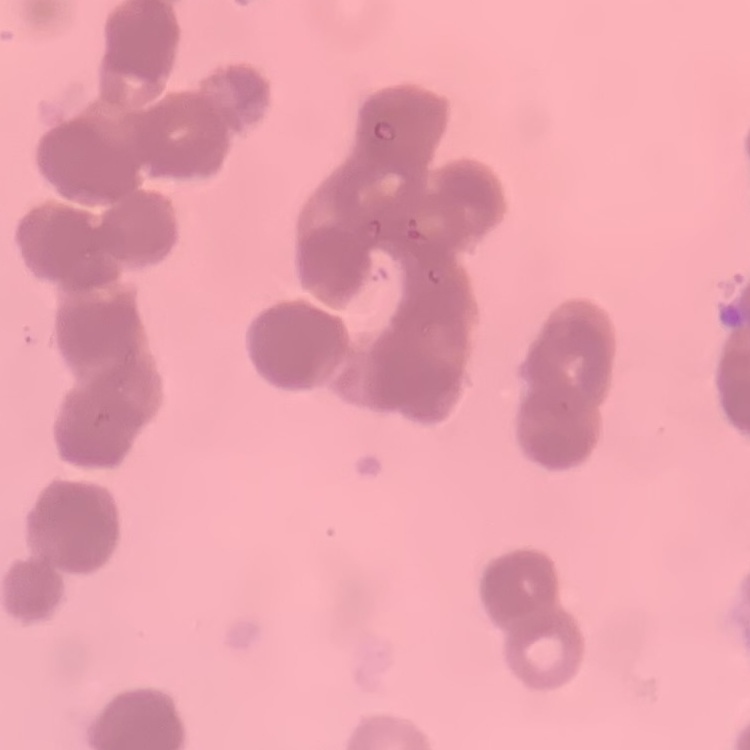

{
  "erythrocyte_morphology": "rouleaux formation",
  "stain": "Field's or Giemsa",
  "preparation": "thin blood smear",
  "image_type": "one tile cut from a larger photomicrograph"
}